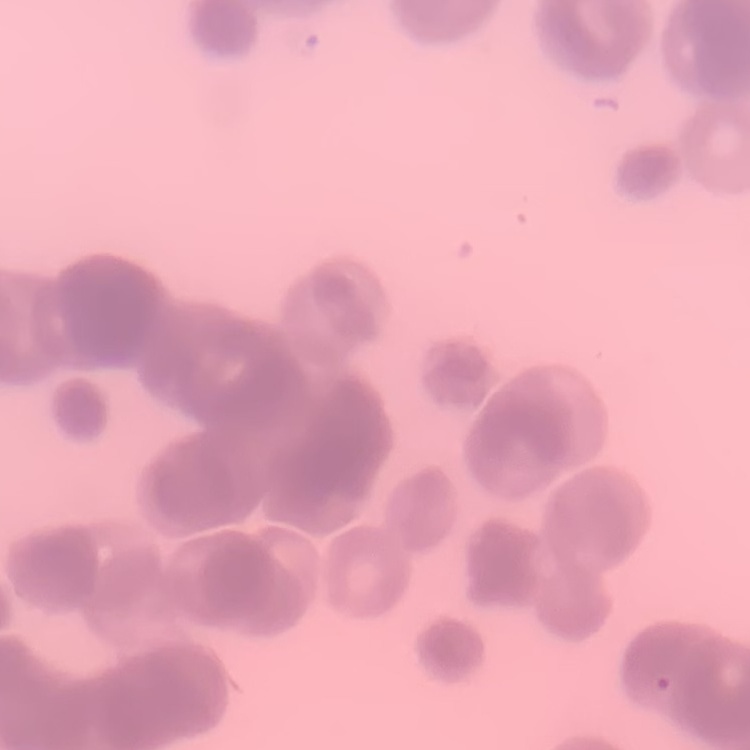
The red blood cells show rouleaux formation. Stained with either Field's or Giemsa. One tile cut from a larger photomicrograph. Thin blood smear.